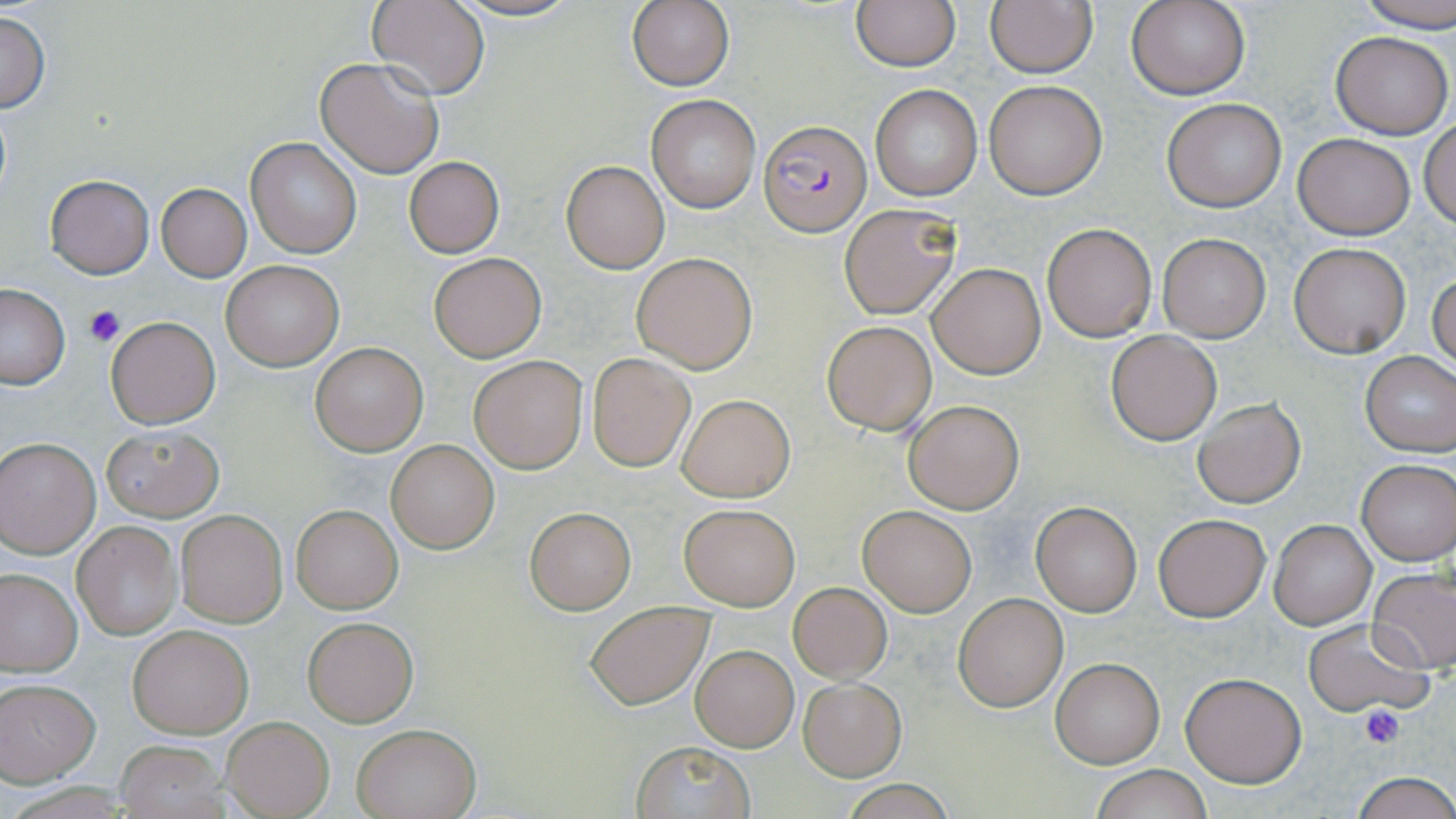

Summary:
  - Coordinate format: approximate bounding boxes as [x1, y1, x2, y2] in pixels
  - Plasmodium falciparum-infected red blood cell locations: [760, 120, 872, 235]
  - Platelet locations: [83, 305, 128, 349], [1358, 703, 1405, 749]
  - Uninfected red blood cell locations: [366, 0, 491, 100], [447, 0, 583, 22], [626, 0, 736, 91], [1357, 0, 1456, 31], [851, 1, 960, 71], [1125, 1, 1251, 102], [984, 3, 1098, 77], [0, 8, 50, 115], [1329, 30, 1454, 139], [315, 57, 443, 178], [984, 80, 1108, 199], [868, 85, 983, 201], [647, 95, 760, 212], [1161, 98, 1287, 211], [1418, 118, 1456, 230], [1292, 133, 1414, 238], [245, 137, 361, 258], [404, 156, 505, 257], [561, 161, 669, 273], [45, 175, 154, 279], [155, 183, 252, 280], [839, 204, 961, 319], [1040, 223, 1157, 340], [1158, 233, 1270, 342], [1289, 243, 1410, 357], [427, 250, 546, 363], [630, 251, 758, 374], [221, 260, 345, 370], [928, 263, 1045, 378], [1429, 270, 1455, 374], [0, 282, 70, 389], [105, 317, 220, 427], [823, 322, 936, 434], [1105, 330, 1222, 444], [308, 341, 428, 457], [1359, 350, 1456, 456], [587, 353, 695, 471], [469, 355, 588, 473], [677, 394, 795, 502], [1192, 397, 1306, 509], [903, 398, 1024, 514], [100, 424, 223, 521], [0, 437, 101, 557], [385, 438, 499, 554], [1356, 459, 1455, 564], [1030, 500, 1143, 617], [678, 503, 799, 610], [857, 503, 978, 617], [291, 505, 402, 613], [525, 507, 636, 614], [174, 509, 287, 627], [1151, 512, 1271, 622], [1270, 520, 1375, 629], [72, 522, 183, 640], [1369, 567, 1456, 674], [0, 568, 82, 677], [789, 582, 892, 683], [953, 594, 1067, 712], [585, 600, 712, 708], [303, 617, 418, 727], [1304, 619, 1433, 718], [126, 624, 253, 737], [690, 645, 798, 751], [1050, 657, 1164, 768], [1180, 673, 1306, 788], [798, 677, 905, 781], [0, 680, 100, 784], [222, 716, 334, 818], [351, 724, 481, 819], [112, 740, 229, 816], [629, 741, 756, 819], [1090, 764, 1212, 819], [1348, 773, 1456, 819], [839, 781, 958, 818]
  - Slide-level diagnosis: Plasmodium falciparum
  - Field of view: one of a larger specimen
  - Stain: May-Grünwald-Giemsa
  - Magnification: 1000x
  - Preparation: thin blood smear
  - Image size: 1456×819 pixels
  - Modality: light microscopy